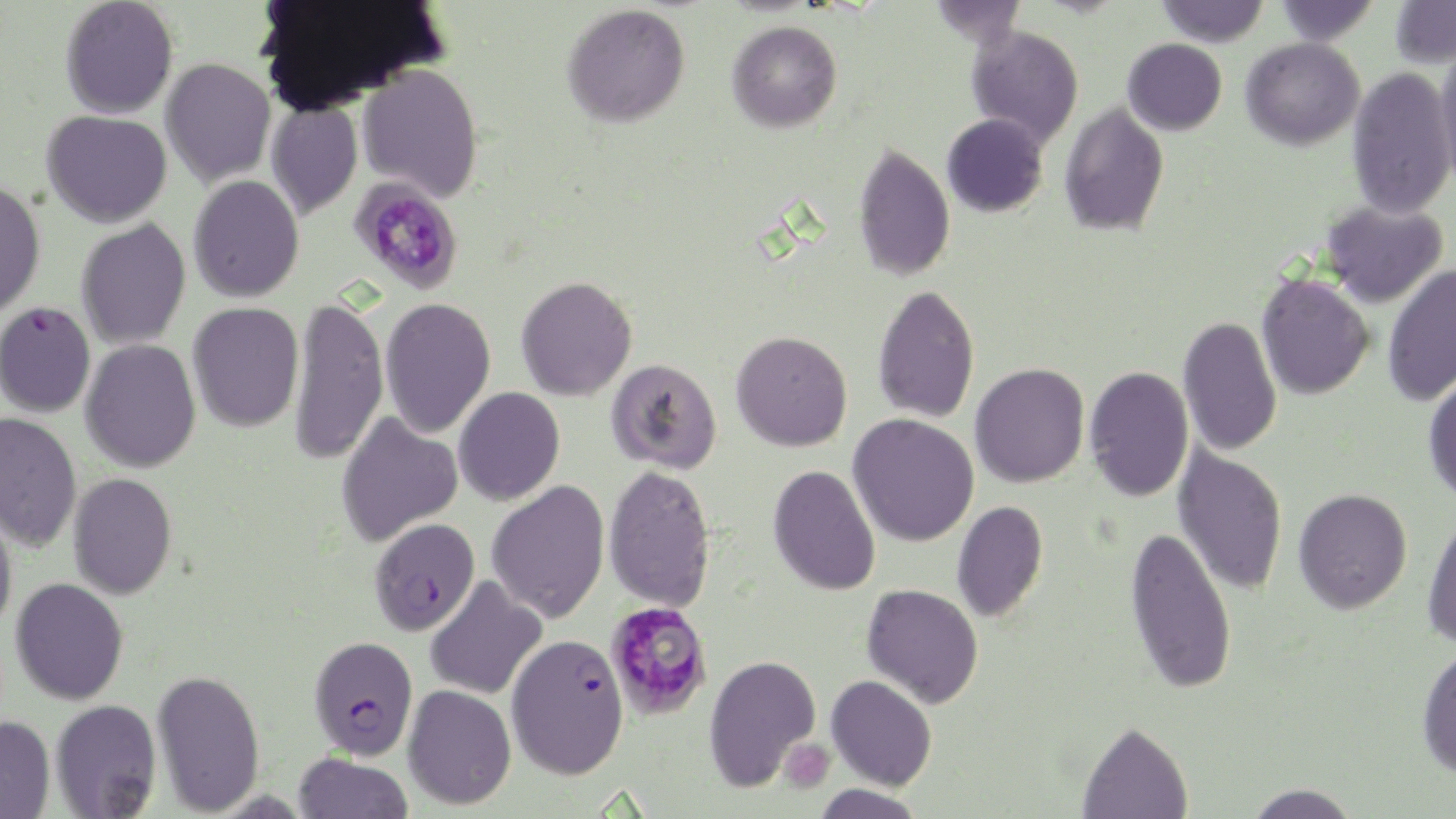
Summary:
  - Coordinate format: approximate bounding boxes as [x1, y1, x2, y2] in pixels
  - Plasmodium falciparum-infected red blood cell locations: [0, 302, 96, 417], [369, 517, 480, 636], [309, 636, 418, 760], [502, 638, 625, 783]
  - Platelet locations: [779, 739, 835, 792]
  - Uninfected red blood cell locations: [60, 0, 179, 119], [927, 0, 1028, 46], [1155, 0, 1270, 46], [1273, 0, 1380, 45], [1389, 1, 1456, 69], [562, 3, 690, 127], [727, 20, 842, 132], [966, 25, 1084, 147], [1240, 37, 1365, 150], [1122, 39, 1227, 136], [1434, 46, 1456, 189], [160, 58, 276, 189], [357, 63, 483, 201], [1347, 67, 1455, 220], [266, 100, 363, 221], [1059, 101, 1169, 237], [42, 110, 172, 228], [942, 113, 1049, 217], [853, 143, 955, 281], [188, 175, 304, 303], [0, 179, 46, 319], [1321, 201, 1448, 308], [76, 218, 191, 350], [1382, 263, 1456, 409], [1256, 274, 1374, 400], [516, 276, 637, 401], [872, 284, 980, 423], [289, 295, 389, 467], [380, 297, 496, 439], [187, 302, 304, 432], [1178, 315, 1282, 456], [731, 331, 852, 451], [80, 340, 201, 473], [606, 358, 722, 473], [970, 362, 1090, 488], [1085, 366, 1194, 502], [1422, 372, 1456, 505], [453, 387, 566, 506], [336, 410, 463, 548], [0, 412, 82, 552], [848, 414, 979, 547], [1173, 445, 1288, 596], [604, 464, 716, 612], [768, 465, 881, 596], [68, 473, 177, 599], [487, 480, 610, 624], [1294, 488, 1412, 614], [0, 499, 18, 636], [951, 501, 1048, 622], [1422, 511, 1456, 651], [1125, 525, 1237, 694], [425, 576, 547, 700], [10, 578, 128, 705], [861, 584, 984, 708], [1416, 644, 1456, 779], [703, 653, 821, 792], [152, 668, 265, 816], [826, 675, 937, 790], [403, 684, 516, 809], [50, 699, 161, 818], [0, 716, 55, 818], [1077, 720, 1193, 818], [293, 752, 413, 818], [1243, 782, 1362, 819], [812, 783, 927, 819]
  - Slide-level diagnosis: Plasmodium falciparum
  - Magnification: 1000x
  - Preparation: thin blood smear
  - Field of view: single
  - Stain: May-Grünwald-Giemsa
  - Modality: light microscopy
  - Image size: 1456×819 pixels